Evaluate for malaria.
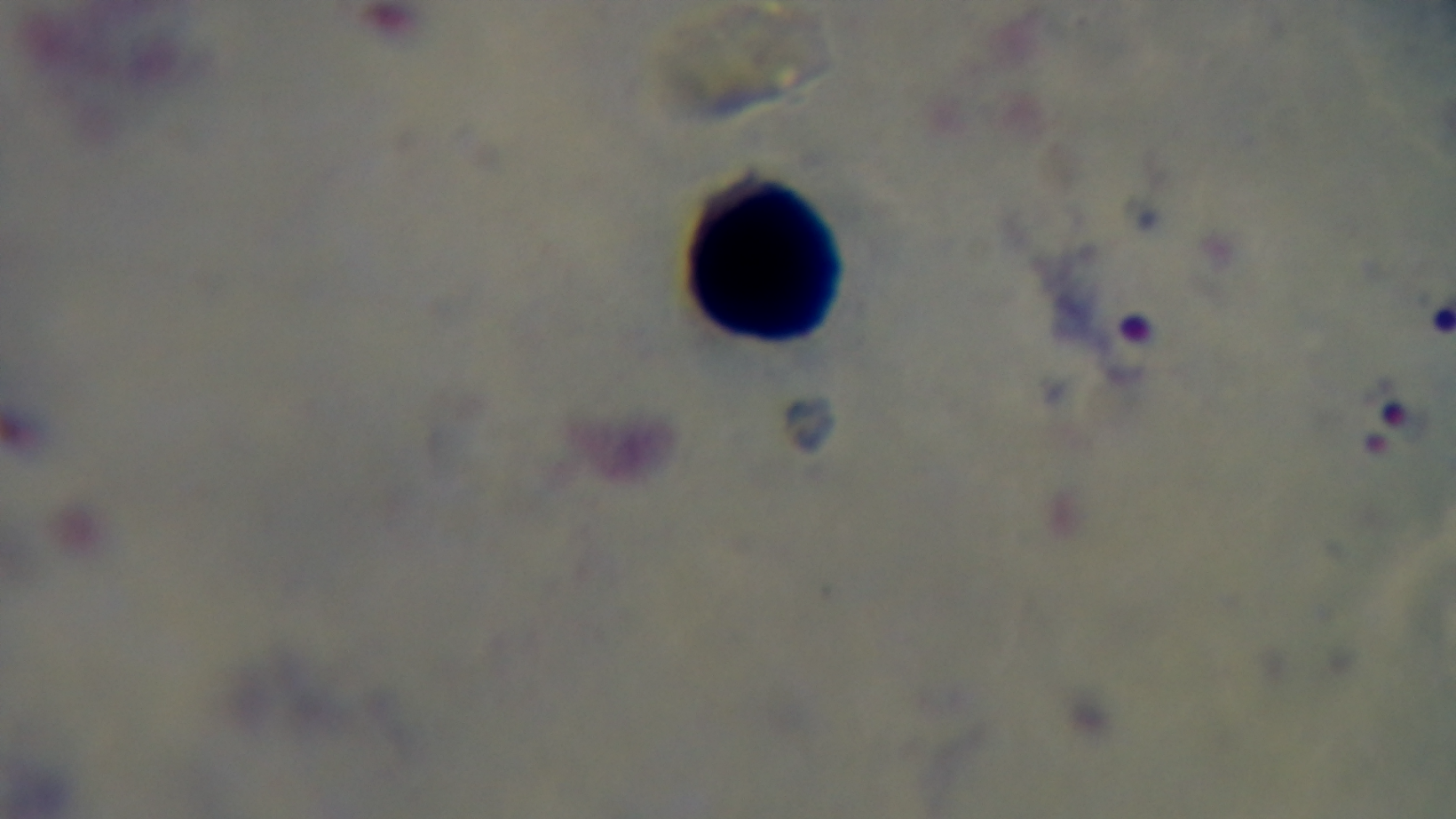
Positive.

field of view = single
capture = mounted 4K digital camera
modality = light microscopy
preparation = thick
stain = Giemsa
objective = 100x oil immersion